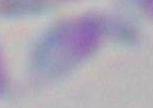 Toxoplasma gondii is seen. Captured at 1000x magnification. Micrograph.